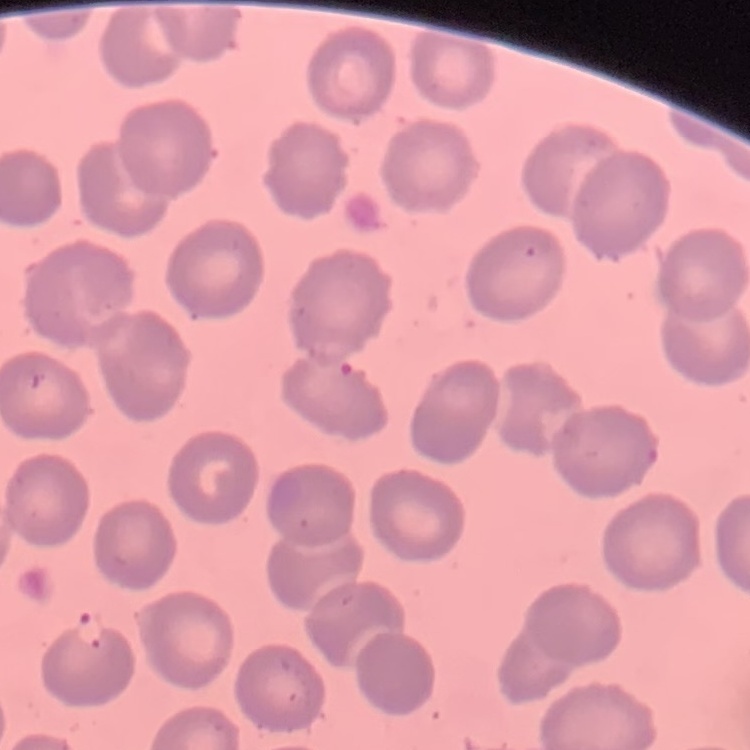
The red blood cells show no rouleaux formation. Field's or Giemsa stain. Thin peripheral smear. Square crop of a larger photomicrograph.